Locate every blood parasite and identify its species.
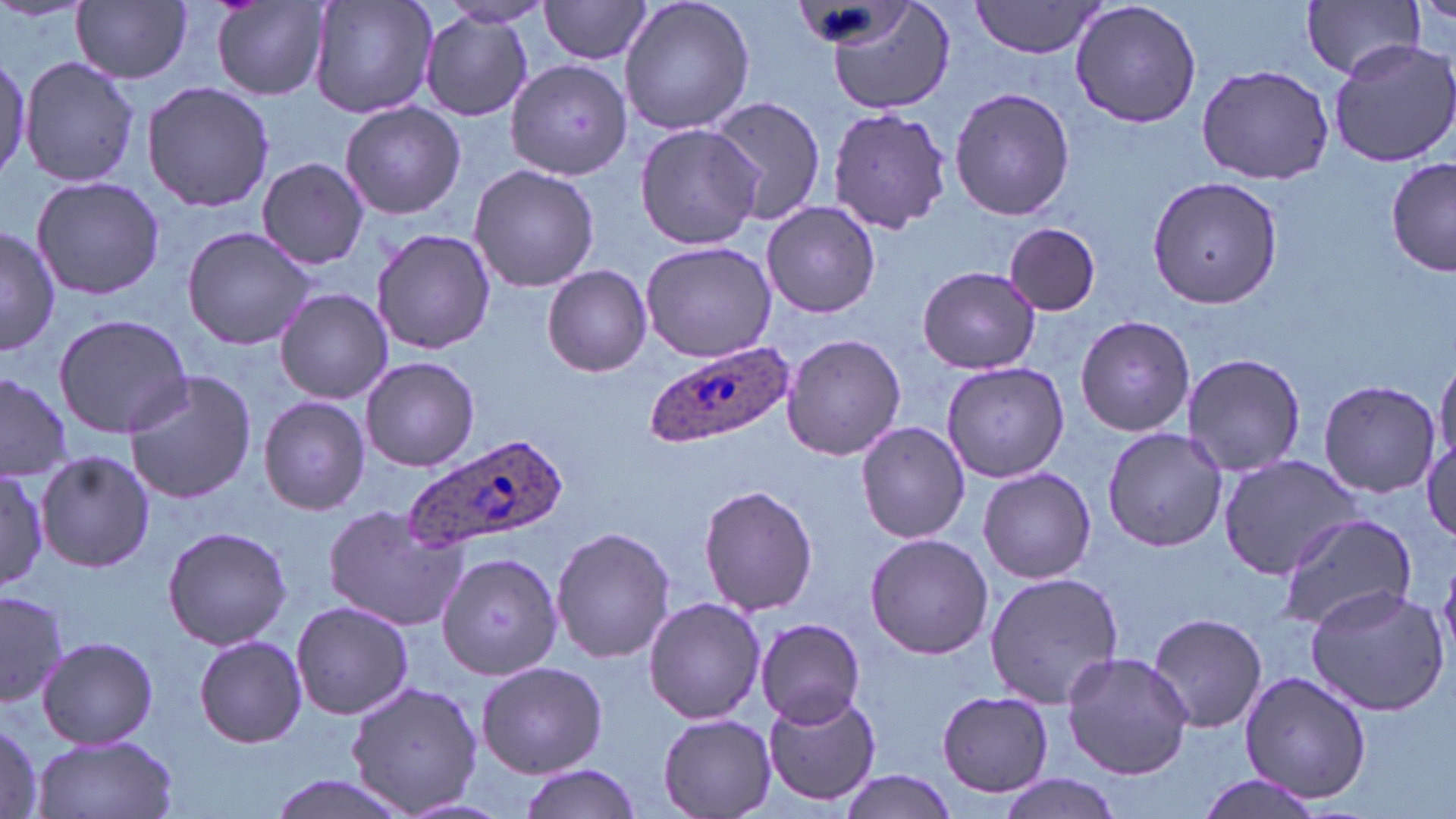

Approximate bounding boxes as named x1/y1/x2/y2 corners in pixels.
Plasmodium ovale-infected red blood cells: (x1=649, y1=339, x2=795, y2=447), (x1=401, y1=432, x2=564, y2=552).
No Plasmodium falciparum, Plasmodium malariae, Plasmodium vivax, Babesia divergens, or Trypanosoma brucei observed.

Summary:
  - Uninfected red blood cell locations: (x1=307, y1=0, x2=440, y2=118), (x1=538, y1=0, x2=655, y2=65), (x1=618, y1=0, x2=755, y2=135), (x1=822, y1=0, x2=956, y2=113), (x1=1069, y1=0, x2=1204, y2=130), (x1=1302, y1=0, x2=1425, y2=79), (x1=72, y1=1, x2=192, y2=84), (x1=972, y1=1, x2=1104, y2=58), (x1=213, y1=2, x2=330, y2=99), (x1=435, y1=2, x2=553, y2=30), (x1=418, y1=14, x2=535, y2=123), (x1=1327, y1=39, x2=1456, y2=170), (x1=0, y1=51, x2=29, y2=186), (x1=20, y1=57, x2=141, y2=189), (x1=505, y1=59, x2=634, y2=182), (x1=1195, y1=64, x2=1336, y2=184), (x1=141, y1=80, x2=275, y2=212), (x1=949, y1=86, x2=1075, y2=222), (x1=704, y1=94, x2=828, y2=226), (x1=339, y1=102, x2=466, y2=220), (x1=825, y1=105, x2=953, y2=236), (x1=635, y1=123, x2=765, y2=250), (x1=257, y1=157, x2=370, y2=270), (x1=1387, y1=159, x2=1455, y2=278), (x1=469, y1=163, x2=599, y2=292), (x1=1146, y1=174, x2=1284, y2=309), (x1=30, y1=175, x2=165, y2=300), (x1=761, y1=200, x2=881, y2=318), (x1=1003, y1=223, x2=1101, y2=315), (x1=0, y1=226, x2=60, y2=355), (x1=181, y1=227, x2=317, y2=351), (x1=371, y1=228, x2=496, y2=355), (x1=641, y1=241, x2=775, y2=361), (x1=542, y1=265, x2=652, y2=377), (x1=917, y1=265, x2=1042, y2=375), (x1=274, y1=289, x2=394, y2=403), (x1=54, y1=313, x2=193, y2=437), (x1=1075, y1=314, x2=1196, y2=437), (x1=782, y1=333, x2=907, y2=462), (x1=1182, y1=351, x2=1306, y2=478), (x1=360, y1=356, x2=479, y2=472), (x1=1434, y1=357, x2=1455, y2=475), (x1=940, y1=361, x2=1071, y2=482), (x1=0, y1=370, x2=72, y2=484), (x1=123, y1=371, x2=259, y2=505), (x1=1317, y1=379, x2=1441, y2=498), (x1=259, y1=396, x2=371, y2=516), (x1=856, y1=421, x2=973, y2=544), (x1=1101, y1=426, x2=1227, y2=552), (x1=1421, y1=437, x2=1456, y2=543), (x1=35, y1=449, x2=154, y2=574), (x1=1219, y1=454, x2=1361, y2=577), (x1=977, y1=468, x2=1098, y2=583), (x1=0, y1=470, x2=49, y2=588), (x1=698, y1=483, x2=819, y2=616), (x1=323, y1=504, x2=466, y2=630), (x1=1275, y1=513, x2=1417, y2=632), (x1=161, y1=525, x2=293, y2=650), (x1=552, y1=526, x2=675, y2=665), (x1=865, y1=533, x2=993, y2=660), (x1=438, y1=550, x2=562, y2=679), (x1=1440, y1=563, x2=1456, y2=664), (x1=984, y1=570, x2=1124, y2=707), (x1=1304, y1=585, x2=1450, y2=716), (x1=0, y1=589, x2=68, y2=709), (x1=643, y1=597, x2=766, y2=724), (x1=290, y1=600, x2=414, y2=719), (x1=1147, y1=612, x2=1269, y2=734), (x1=755, y1=617, x2=868, y2=729), (x1=36, y1=634, x2=159, y2=749), (x1=193, y1=634, x2=307, y2=748), (x1=1062, y1=651, x2=1194, y2=779), (x1=475, y1=660, x2=608, y2=777), (x1=1236, y1=672, x2=1375, y2=804), (x1=344, y1=679, x2=483, y2=816), (x1=764, y1=689, x2=882, y2=805), (x1=936, y1=690, x2=1055, y2=797), (x1=658, y1=714, x2=775, y2=816), (x1=0, y1=720, x2=44, y2=818), (x1=31, y1=733, x2=180, y2=819), (x1=519, y1=765, x2=641, y2=819), (x1=836, y1=770, x2=959, y2=817), (x1=264, y1=774, x2=414, y2=819), (x1=995, y1=775, x2=1125, y2=819), (x1=1190, y1=775, x2=1327, y2=819)
  - Slide-level diagnosis: Plasmodium ovale
  - Field of view: single
  - Modality: light microscopy
  - Magnification: 1000x
  - Image size: 1456×819 pixels
  - Stain: May-Grünwald-Giemsa
  - Preparation: thin blood film